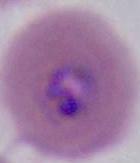
Summary:
  - Modality: micrograph
  - Identification: Plasmodium
  - Magnification: 400x or 1000x